Report the malaria status of this cell.
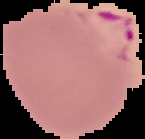

It is parasitized.

Cell region segmented out of the field of view; the surrounding area is masked to black. Image is 145×139 pixels. From a thin blood smear.